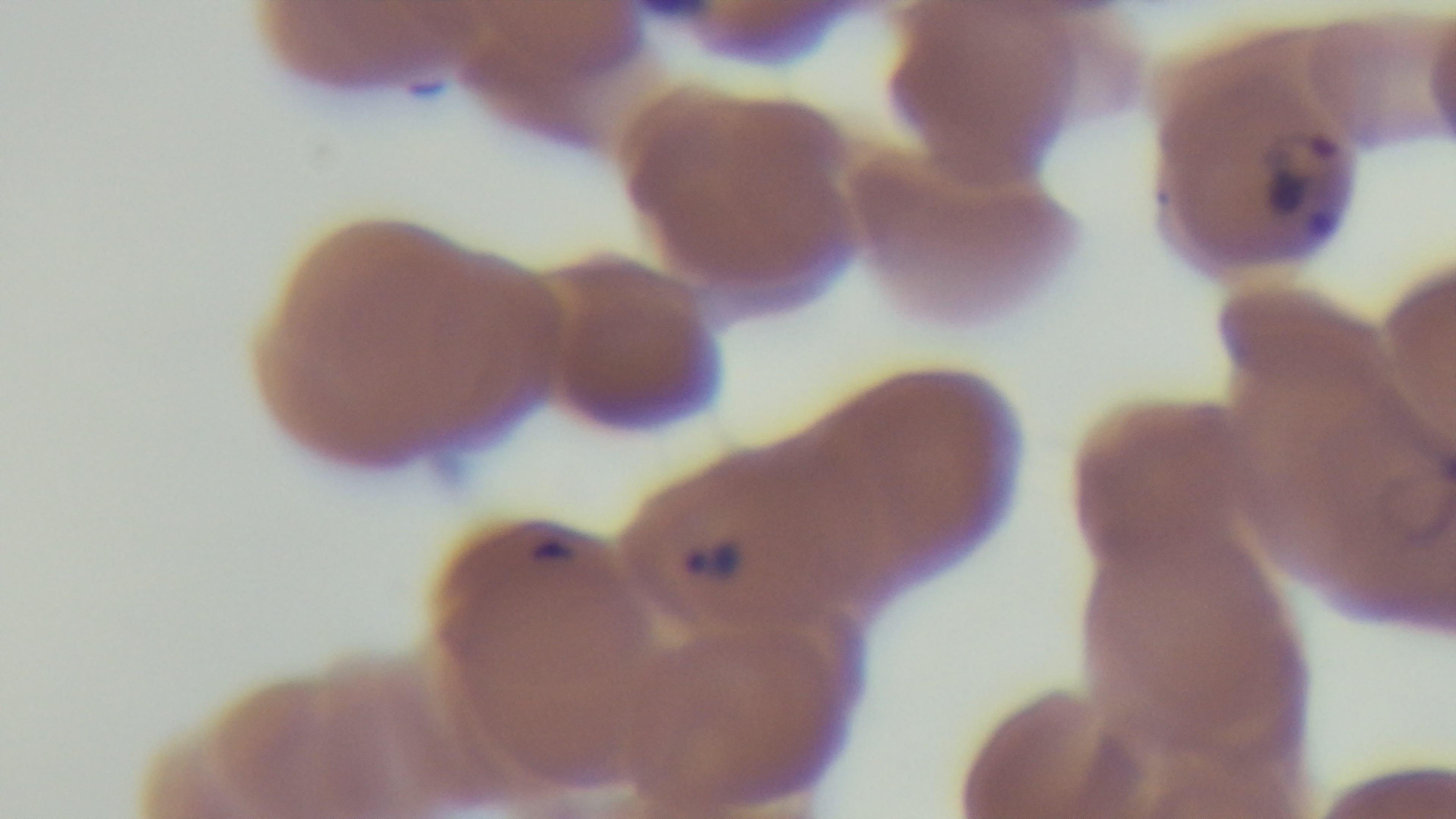
modality: light microscopy
stain: Giemsa
preparation: thin blood film
capture: mounted 4K digital camera
field_of_view: one from the slide
malaria_status: infected
objective: 100x oil immersion